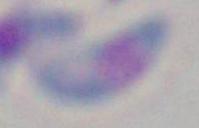 Toxoplasma gondii is seen. Captured at 1000x magnification. Micrograph.